Assess this cell for malaria.
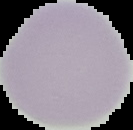
Uninfected.

Segmented cell region on a black background. From a thin blood film. Image is 133×130 pixels.